Locate every blood parasite and identify its species.
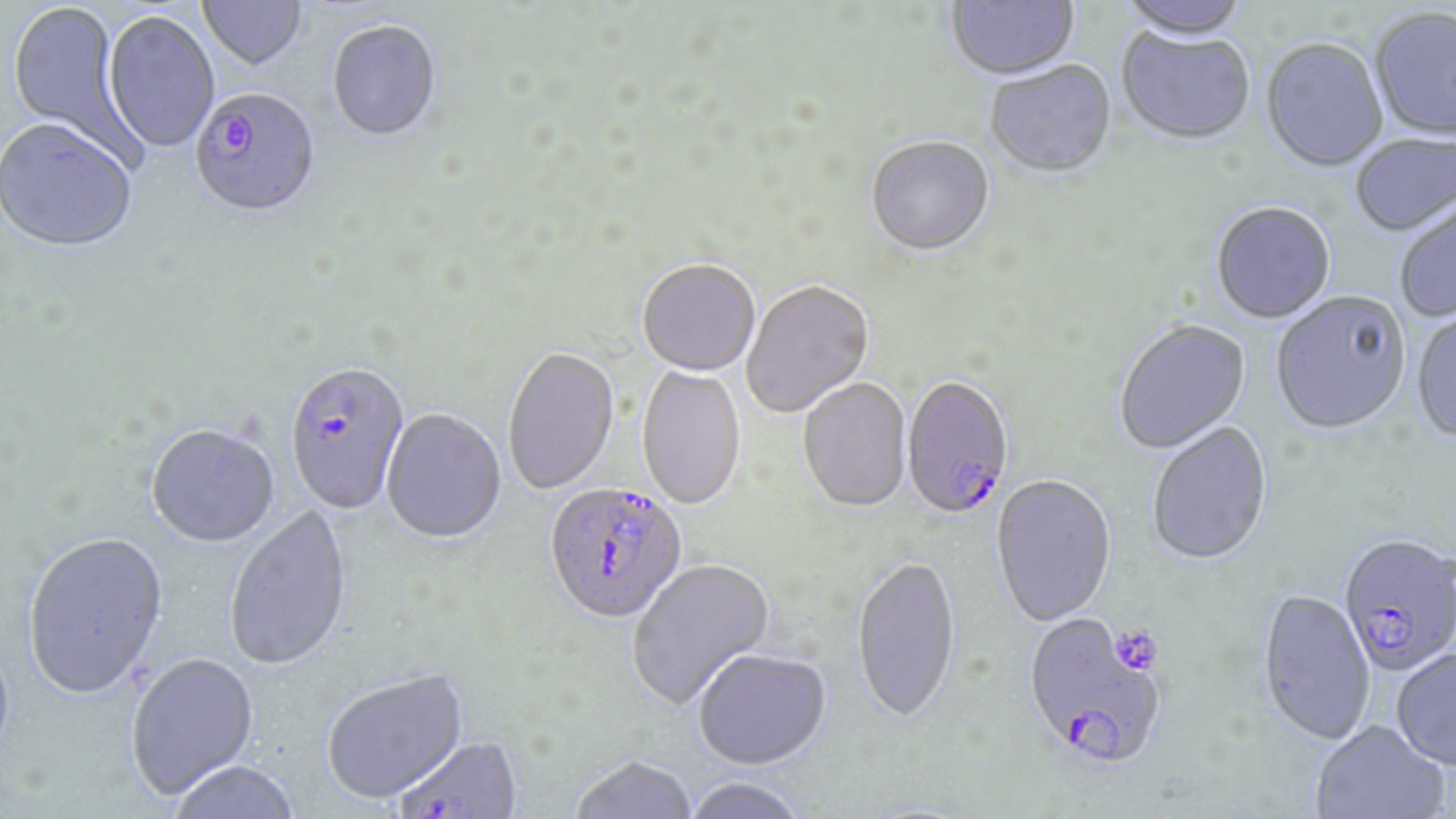

Approximate bounding boxes as (x1, y1, x2, y2) in pixels.
Plasmodium falciparum-infected red blood cells: (188, 89, 320, 221), (285, 366, 410, 517), (900, 379, 1014, 523), (543, 483, 687, 628), (1338, 537, 1456, 680), (1021, 614, 1167, 775), (394, 738, 524, 819).
No Plasmodium ovale, Plasmodium malariae, Plasmodium vivax, Babesia divergens, or Trypanosoma brucei observed.

Uninfected red blood cell locations: (198, 0, 308, 74), (945, 0, 1080, 84), (1116, 0, 1254, 45), (7, 1, 138, 158), (1369, 9, 1456, 144), (103, 11, 220, 155), (327, 22, 442, 143), (1116, 29, 1255, 148), (1260, 40, 1388, 175), (984, 62, 1117, 181), (0, 122, 138, 256), (1350, 134, 1455, 238), (866, 138, 994, 258), (1395, 196, 1456, 323), (1210, 203, 1336, 325), (637, 261, 760, 378), (742, 281, 875, 418), (1271, 294, 1411, 437), (1411, 310, 1456, 445), (1114, 321, 1252, 456), (502, 348, 620, 496), (636, 365, 747, 512), (798, 379, 912, 515), (380, 410, 506, 546), (1147, 422, 1273, 569), (145, 425, 280, 550), (990, 476, 1117, 629), (224, 505, 354, 674), (21, 533, 170, 703), (851, 557, 961, 730), (626, 558, 776, 711), (1257, 591, 1375, 748), (0, 637, 16, 773), (1391, 649, 1456, 774), (693, 651, 831, 772), (125, 653, 260, 802), (321, 669, 470, 807), (1310, 722, 1449, 819), (568, 756, 697, 819), (168, 762, 301, 819), (680, 779, 811, 819). Slide-level diagnosis: Plasmodium falciparum. One field of a larger specimen. May-Grünwald-Giemsa stain. Optical microscopy. Image is 1456×819 pixels. 1000x magnification. Thin blood film.